Name the blood parasite species.
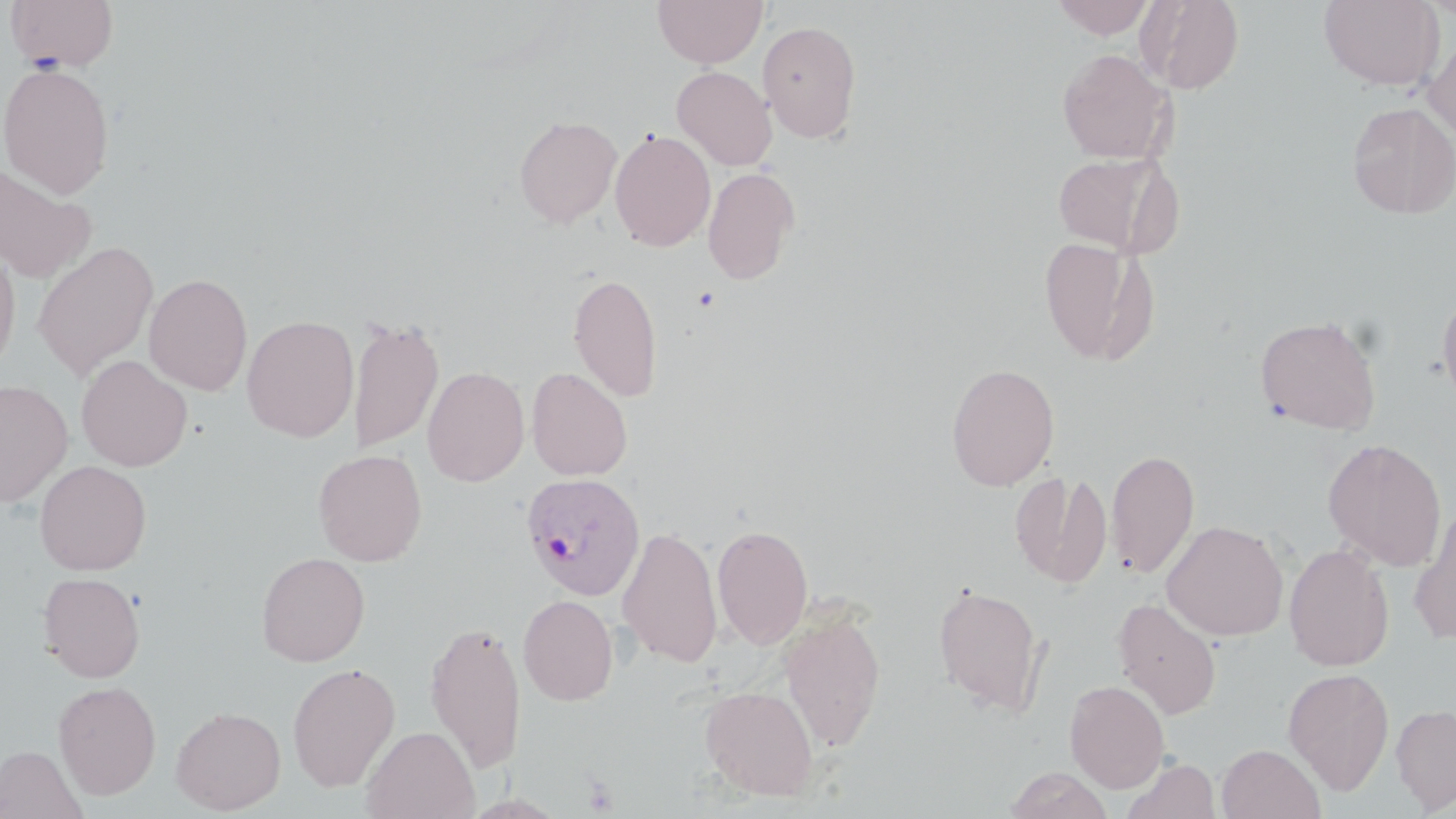

Plasmodium ovale.

Summary:
  - Coordinate format: approximate bounding boxes as (x1,y1)-(x2,y2) corner pairs in pixels
  - Platelet locations: (583,776)-(619,814)
  - Plasmodium ovale-infected red blood cell locations: (521,472)-(646,600)
  - Uninfected red blood cell locations: (5,0)-(119,72), (652,0)-(767,68), (1050,0)-(1158,39), (1138,0)-(1244,94), (1319,0)-(1445,91), (758,20)-(862,143), (1423,34)-(1456,144), (1056,48)-(1177,164), (0,61)-(116,198), (671,66)-(777,171), (1348,101)-(1456,219), (514,115)-(622,228), (609,129)-(716,252), (1051,151)-(1180,257), (0,163)-(97,284), (702,166)-(800,285), (1038,236)-(1153,364), (32,241)-(158,380), (0,244)-(20,376), (568,272)-(663,402), (144,273)-(253,396), (1437,286)-(1456,412), (1255,313)-(1382,434), (242,314)-(359,442), (346,316)-(444,454), (76,355)-(192,472), (946,363)-(1060,490), (422,366)-(529,487), (526,367)-(632,481), (0,379)-(73,507), (1322,437)-(1447,571), (1107,447)-(1200,580), (313,448)-(427,566), (34,460)-(151,575), (1011,469)-(1111,589), (1409,507)-(1456,643), (1161,519)-(1289,641), (711,523)-(813,650), (618,525)-(723,668), (1284,543)-(1395,671), (256,551)-(370,666), (38,572)-(145,683), (932,582)-(1047,716), (518,594)-(619,706), (1113,597)-(1222,719), (779,610)-(886,752), (425,620)-(528,772), (287,661)-(400,792), (1283,668)-(1394,795), (53,680)-(161,799), (1064,680)-(1170,793), (700,684)-(819,800), (1391,704)-(1456,813), (170,706)-(286,814), (21,721)-(145,814), (361,725)-(479,819), (1217,743)-(1325,819), (0,744)-(88,819), (1121,758)-(1220,819), (1004,767)-(1113,818)
  - Magnification: 1000x
  - Preparation: thin blood smear
  - Field of view: single
  - Stain: May-Grünwald-Giemsa
  - Image size: 1456×819 pixels
  - Modality: light microscopy